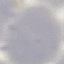
Summary:
  - Result: negative for malaria parasites
  - Preparation: thin blood film
  - Stain: Giemsa
  - Image type: automatically extracted cell patch, resized to 64 × 64 pixels
  - Capture: smartphone through the microscope eyepiece